Identify the parasite.
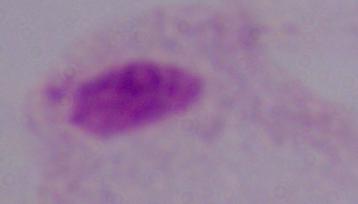

A trichomonad.

Summary:
  - Magnification: 1000x
  - Modality: photomicrograph